Locate and identify every blood parasite.
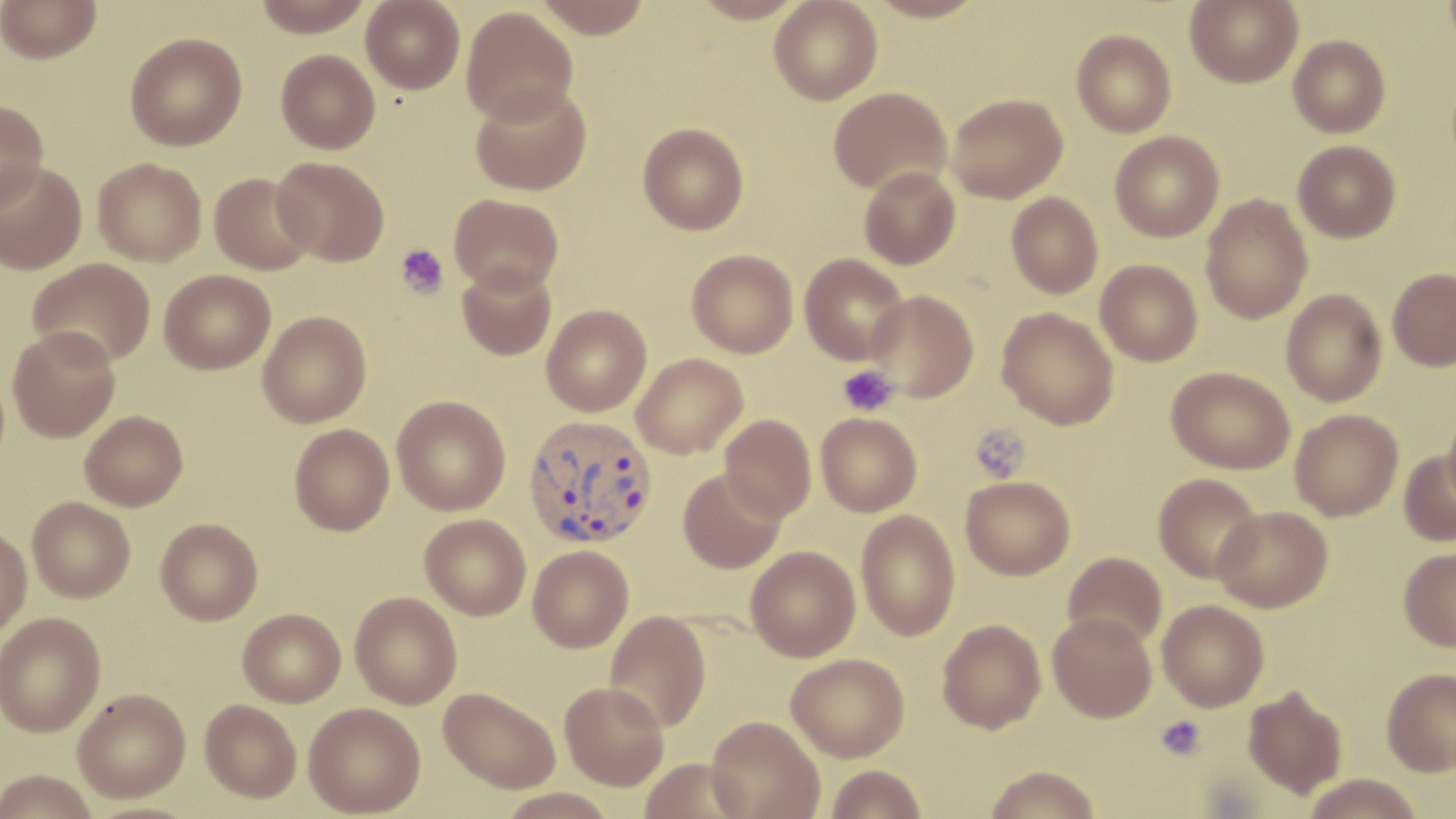
Approximate bounding boxes as (x1, y1, x2, y2) in pixels.
Plasmodium vivax-infected red blood cells: (524, 415, 658, 549).
No Plasmodium falciparum, Plasmodium ovale, Plasmodium malariae, Babesia divergens, or Trypanosoma brucei observed.

slide-level diagnosis = Plasmodium vivax
magnification = 1000x
image size = 1456×819 pixels
field of view = single
platelet locations = approximate bounding boxes as (x1, y1, x2, y2) in pixels: (395, 244, 448, 300), (837, 364, 898, 417), (969, 423, 1031, 483), (1156, 715, 1207, 760)
stain = May-Grünwald-Giemsa
modality = light microscopy
preparation = thin blood smear
uninfected red blood cell locations = approximate bounding boxes as (x1, y1, x2, y2) in pixels: (1, 0, 101, 63), (251, 0, 375, 37), (361, 0, 465, 94), (531, 0, 654, 38), (769, 0, 882, 105), (866, 0, 987, 23), (1185, 0, 1303, 88), (1441, 0, 1456, 59), (461, 6, 578, 125), (1071, 30, 1176, 138), (125, 32, 247, 151), (1288, 35, 1391, 138), (276, 49, 380, 153), (471, 82, 592, 195), (828, 87, 952, 196), (947, 93, 1068, 204), (0, 99, 49, 211), (637, 122, 749, 235), (1110, 131, 1224, 242), (1293, 140, 1401, 244), (272, 156, 390, 266), (93, 157, 207, 266), (0, 161, 87, 275), (859, 166, 961, 269), (209, 172, 316, 275), (1006, 192, 1103, 298), (449, 194, 564, 295), (1201, 195, 1313, 324), (686, 249, 798, 358), (800, 253, 909, 365), (28, 258, 155, 368), (1095, 259, 1203, 366), (457, 263, 557, 360), (1387, 268, 1456, 371), (159, 269, 276, 374), (1281, 289, 1387, 406), (866, 290, 979, 402), (542, 305, 651, 416), (997, 307, 1119, 429), (258, 310, 372, 427), (7, 326, 120, 442), (631, 353, 748, 459), (1167, 366, 1295, 474), (392, 395, 511, 516), (1290, 409, 1403, 521), (1443, 409, 1456, 513), (80, 410, 188, 511), (816, 413, 922, 516), (719, 414, 816, 521), (289, 424, 394, 535), (1398, 448, 1456, 548), (678, 469, 787, 574), (1153, 473, 1263, 584), (960, 475, 1075, 580), (27, 496, 135, 602), (1212, 506, 1333, 613), (856, 509, 961, 642), (420, 514, 531, 620), (155, 518, 263, 625), (0, 525, 32, 638), (528, 545, 633, 652), (745, 546, 860, 662), (1398, 548, 1456, 651), (1062, 552, 1167, 650), (350, 591, 462, 709), (1157, 599, 1269, 711), (238, 608, 346, 706), (605, 611, 712, 733), (0, 612, 106, 737), (1048, 612, 1157, 723), (937, 619, 1046, 734), (785, 654, 909, 761), (1382, 668, 1456, 776), (560, 682, 669, 791), (1243, 685, 1348, 800), (439, 686, 561, 793), (73, 688, 191, 802), (200, 698, 302, 802), (303, 702, 425, 817), (706, 715, 825, 819), (639, 758, 749, 818), (826, 764, 927, 818), (982, 765, 1102, 819), (0, 769, 98, 819), (1302, 774, 1424, 818), (496, 787, 620, 818)